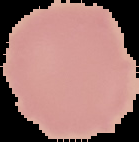

{
  "preparation": "thin blood film",
  "image_type": "segmented cell region with the area outside set to black",
  "image_size": "139×142 pixels",
  "malaria_status": "uninfected"
}